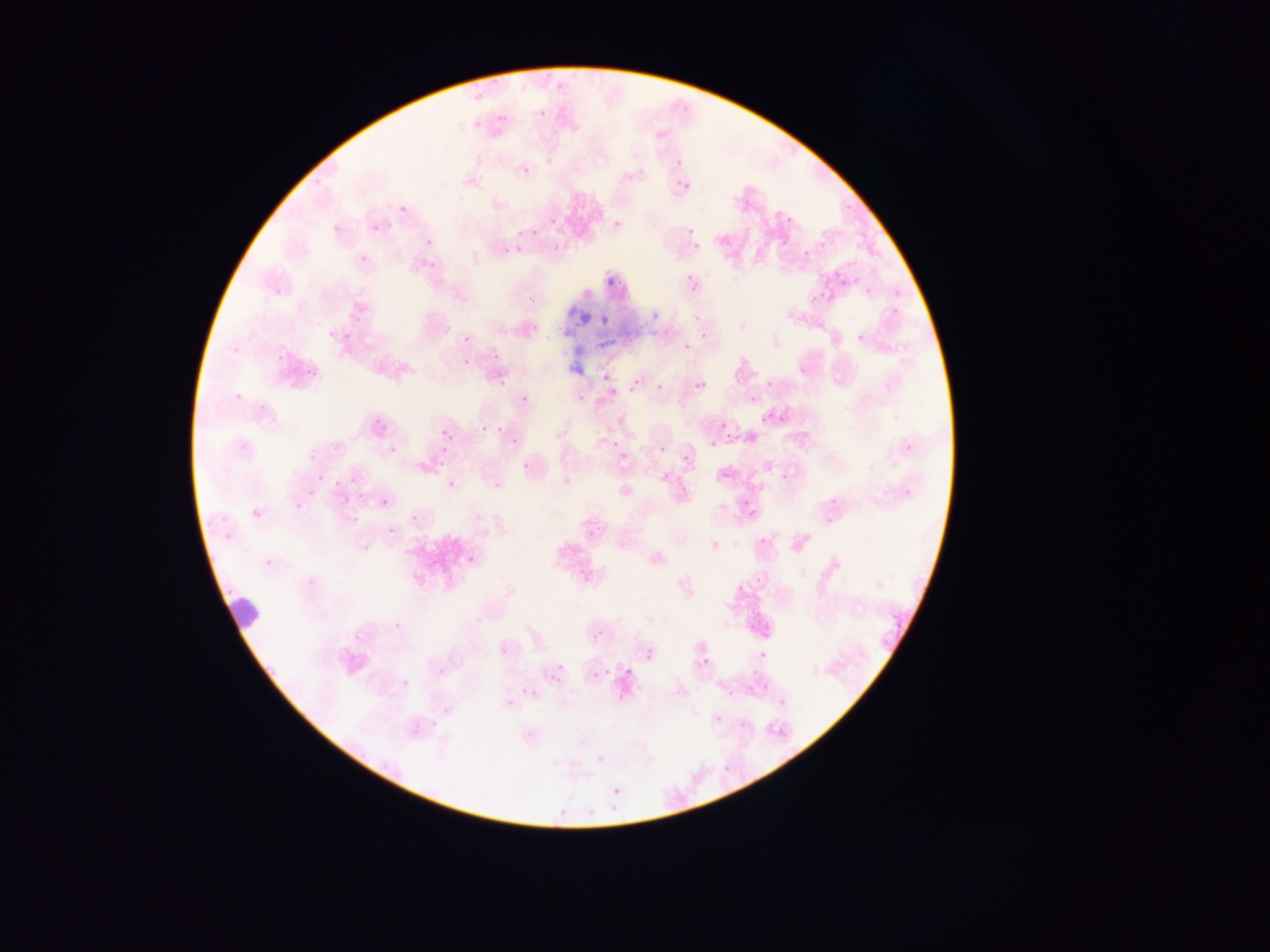
{
  "malaria_parasite_locations": "approximate bounding boxes as left top right bottom in pixels (subset; some below the resolvable size): 471 92 482 102; 674 103 697 122; 538 110 546 117; 497 114 506 124; 473 120 481 129; 674 160 681 168; 522 166 532 175; 681 182 690 190; 398 194 428 217; 777 212 793 231; 365 215 397 245; 549 216 557 224; 325 218 345 241; 677 218 703 240; 531 221 543 243; 714 227 735 247; 517 230 523 239; 550 231 569 247; 793 231 841 260; 425 239 432 247; 694 243 701 251; 500 245 508 253; 847 257 856 268; 827 268 852 292; 682 271 703 290; 607 277 615 284; 521 284 542 303; 864 288 872 296; 811 295 818 303; 886 299 903 315; 651 312 660 321; 800 314 809 323; 599 315 609 324; 527 317 541 338; 687 320 716 340; 852 330 865 342; 343 333 351 342; 465 334 473 342; 596 338 608 349; 489 350 501 359; 463 358 470 366; 288 361 317 387; 498 362 525 387; 601 374 610 382; 633 378 642 389; 696 381 707 391; 765 381 772 389; 654 383 664 392; 524 394 533 402; 748 395 756 404; 779 414 787 424; 373 419 385 429; 720 423 729 432; 480 425 489 433; 723 429 742 445; 443 430 452 439; 513 432 524 446; 611 438 620 447; 709 441 717 449; 432 442 453 469; 379 443 392 457; 679 445 697 464; 522 450 540 470; 620 452 628 460; 781 460 794 476; 311 468 326 481; 447 480 456 489; 489 481 501 494; 814 485 850 530; 285 488 314 518; 339 488 356 502; 361 489 369 505; 379 497 389 507; 740 498 769 525; 347 513 360 530; 410 513 420 524; 386 525 394 537; 752 539 769 554; 351 540 368 556; 574 547 601 590; 467 555 476 565; 748 575 765 595; 875 579 887 590; 591 631 602 643; 644 649 654 660; 751 650 776 660; 697 656 709 669; 394 657 420 684; 749 657 769 674; 554 662 564 672; 603 666 612 676; 624 666 634 675; 552 674 564 684; 526 687 540 699; 718 689 735 704; 494 692 508 713; 769 698 786 710; 712 705 726 719; 408 721 418 737; 427 722 443 734; 716 756 732 774; 612 787 621 796 | approximate x y pixel centers of objects too small to bound: 617 223; 683 348; 662 449",
  "country": "Ghana",
  "preparation": "thin blood smear",
  "leukocyte_locations": "approximate bounding boxes as left top right bottom in pixels: 218 590 264 633",
  "field_of_view": "single",
  "image_size": "1270×952 pixels",
  "capture": "mobile-phone photograph through a microscope"
}